Assess this cell for malaria.
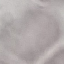
It is uninfected.

capture: smartphone through the microscope eyepiece
preparation: thin blood smear
image_type: automatically extracted cell patch, resized to 64 × 64 pixels
stain: Giemsa